Identify the blood parasite species.
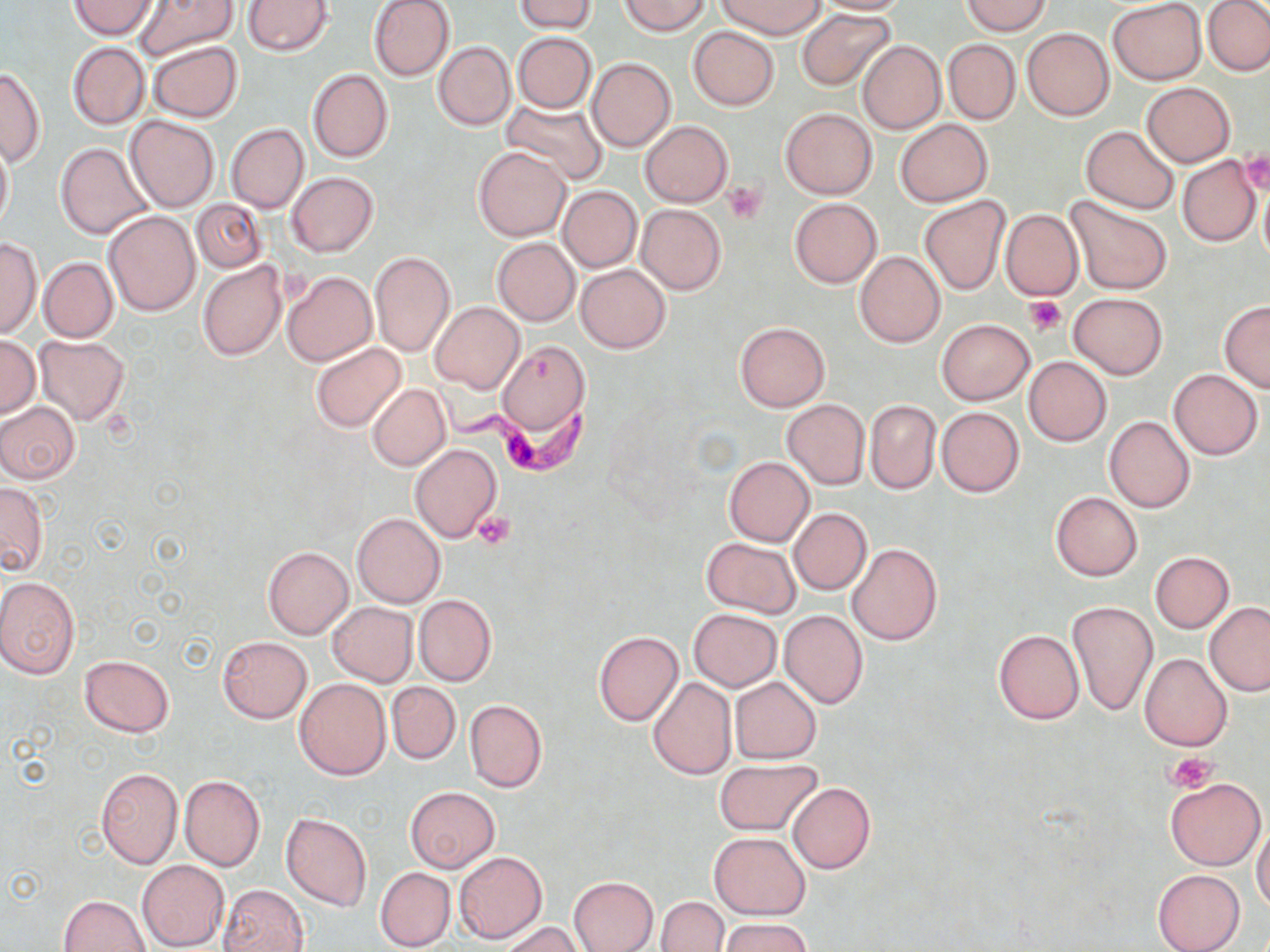

Trypanosoma brucei.

Approximate bounding boxes as [x1, y1, x2, y2] in pixels. Trypanosoma brucei locations: [428, 378, 595, 477]. Uninfected red blood cell locations: [133, 0, 238, 59], [242, 0, 332, 55], [368, 0, 455, 81], [515, 0, 598, 33], [622, 0, 710, 36], [814, 0, 913, 14], [1107, 0, 1206, 85], [1203, 0, 1270, 77], [69, 1, 157, 39], [718, 1, 826, 37], [961, 1, 1052, 35], [796, 9, 894, 91], [688, 26, 779, 111], [1022, 28, 1113, 121], [512, 32, 597, 114], [943, 38, 1020, 124], [857, 40, 945, 134], [432, 41, 515, 130], [67, 42, 149, 129], [149, 42, 242, 122], [586, 57, 677, 152], [0, 66, 45, 165], [308, 68, 393, 162], [1141, 83, 1234, 166], [502, 98, 609, 185], [781, 108, 876, 199], [125, 116, 218, 212], [896, 118, 992, 206], [640, 120, 733, 207], [226, 123, 308, 214], [1081, 126, 1179, 213], [0, 137, 13, 235], [55, 143, 152, 239], [473, 146, 570, 241], [1177, 154, 1261, 247], [286, 172, 379, 256], [1258, 174, 1270, 271], [558, 185, 642, 272], [918, 197, 1009, 295], [1065, 197, 1172, 295], [790, 198, 882, 287], [192, 199, 266, 272], [635, 204, 726, 294], [1000, 209, 1083, 301], [104, 211, 199, 315], [491, 237, 580, 326], [0, 238, 43, 338], [369, 251, 456, 357], [854, 251, 946, 347], [40, 258, 117, 341], [199, 262, 287, 361], [576, 264, 670, 353], [281, 272, 375, 366], [1069, 293, 1167, 379], [429, 301, 526, 393], [1219, 302, 1270, 392], [937, 319, 1034, 405], [734, 322, 829, 412], [0, 335, 40, 418], [35, 336, 129, 424], [498, 339, 590, 438], [310, 342, 406, 433], [1024, 356, 1111, 445], [1168, 369, 1263, 460], [367, 384, 450, 470], [782, 400, 869, 491], [866, 400, 940, 494], [0, 402, 80, 484], [936, 406, 1025, 496], [1105, 416, 1194, 513], [408, 444, 501, 542], [723, 456, 814, 547], [1, 481, 49, 576], [1050, 491, 1142, 580], [789, 508, 871, 595], [352, 513, 446, 607], [702, 537, 800, 616], [847, 544, 942, 645], [262, 546, 352, 639], [1150, 551, 1233, 633], [0, 577, 79, 679], [414, 595, 496, 686], [1068, 601, 1157, 716], [1204, 601, 1270, 695], [328, 602, 417, 686], [688, 609, 780, 691], [779, 611, 868, 709], [993, 629, 1084, 723], [594, 631, 683, 726], [217, 636, 312, 723], [1139, 653, 1231, 750], [79, 655, 174, 737], [730, 676, 821, 763], [294, 677, 391, 780], [646, 677, 737, 781], [387, 682, 460, 764], [465, 699, 546, 792], [713, 758, 822, 836], [95, 768, 182, 868], [179, 775, 265, 871], [1165, 777, 1266, 870], [788, 782, 874, 873], [405, 787, 499, 872], [281, 811, 372, 911], [1252, 824, 1270, 913], [710, 832, 809, 919], [454, 851, 547, 945], [137, 860, 229, 951], [375, 867, 455, 950], [1152, 868, 1243, 951], [568, 876, 658, 952], [218, 884, 309, 952], [59, 895, 150, 951], [657, 896, 727, 952], [718, 918, 812, 952], [500, 921, 585, 952]. Platelet locations: [1239, 150, 1270, 196], [722, 181, 767, 224], [1022, 296, 1066, 334], [473, 510, 517, 550], [1166, 752, 1218, 794]. Light microscopy. Captured at 1000x magnification. May-Grünwald-Giemsa stain. Thin blood film. One field of a larger specimen. Image is 1270×952 pixels.